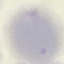

Summary:
  - Result: no malaria parasites seen
  - Preparation: thin blood film
  - Image type: cell patch, automatically extracted from a larger field of view and resized to 64 × 64 pixels
  - Stain: Giemsa
  - Capture: smartphone through the microscope eyepiece